State which parasite is depicted.
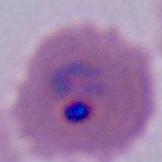

This is Plasmodium.

Micrograph. 400x or 1000x magnification.